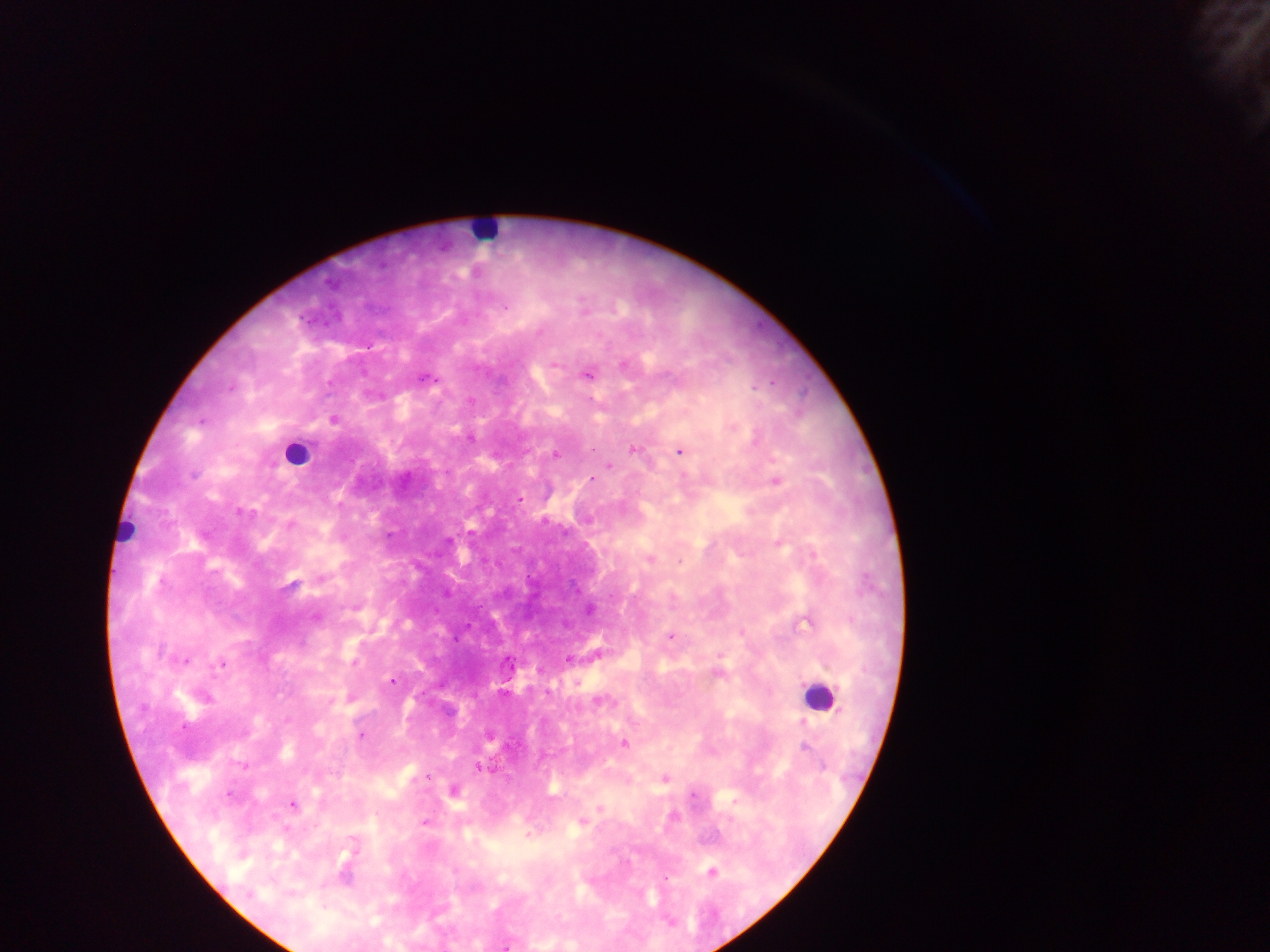
Approximate centers as {x, y} in pixels.
Summary:
  - Malaria parasite locations: {505, 308}, {367, 346}, {555, 364}, {623, 365}, {588, 374}, {425, 378}, {230, 389}, {333, 420}, {201, 421}, {733, 428}, {470, 438}, {592, 449}, {633, 449}, {680, 452}, {557, 454}, {609, 466}, {193, 475}, {591, 479}, {776, 482}, {520, 500}, {240, 512}, {290, 524}, {779, 543}, {650, 559}, {679, 561}, {292, 585}, {589, 610}, {314, 617}, {806, 623}, {670, 637}, {568, 659}, {186, 660}, {221, 664}, {718, 674}, {392, 681}, {577, 683}, {599, 702}, {361, 735}, {624, 744}, {805, 746}, {241, 765}, {481, 769}, {428, 777}, {665, 779}, {228, 795}, {693, 795}, {293, 804}, {600, 808}, {672, 816}, {424, 822}, {581, 822}, {527, 835}, {712, 872}, {666, 878}, {505, 947}
  - Leukocyte locations: {483, 232}, {297, 454}, {126, 531}, {817, 696}
  - Capture: mobile-phone photograph through a microscope
  - Field of view: single
  - Preparation: thick blood film
  - Country: Ghana
  - Image size: 1270×952 pixels